Report the malaria status of this cell.
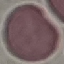

Uninfected.

Summary:
  - Image type: cell patch, automatically extracted from a larger field of view and resized to 64 × 64 pixels
  - Capture: smartphone camera at the microscope eyepiece
  - Stain: Giemsa
  - Preparation: thin blood film